Locate every malaria parasite.
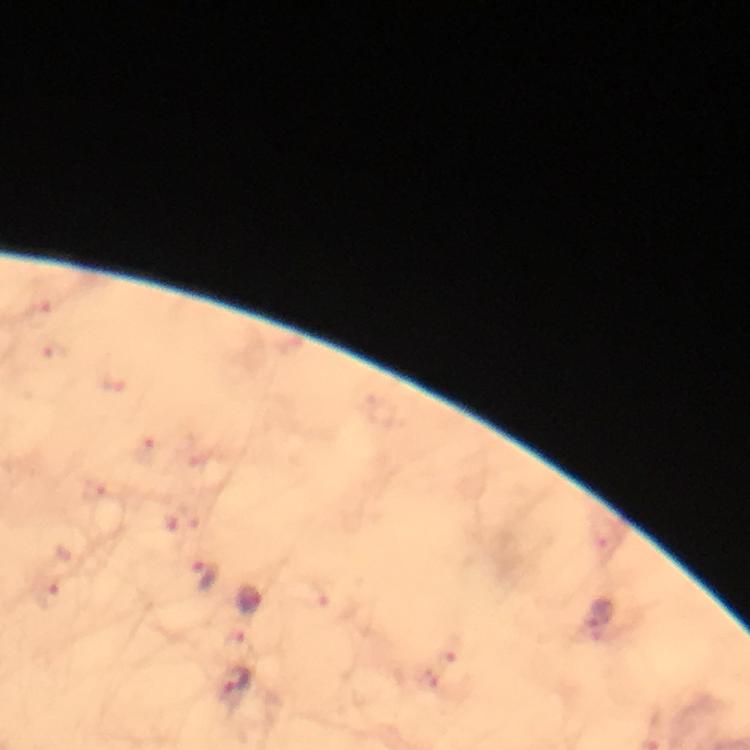
Approximate centers as (x, y) in pixels.
Malaria parasites: (205, 577), (248, 600), (599, 619), (235, 684).

Summary:
  - Magnification: 100x
  - Capture: smartphone mounted on the microscope
  - Preparation: thick blood film
  - Context: from a diagnostic examination for malaria
  - Image size: 750×750 pixels
  - Stain: Giemsa
  - Cropped from: one field of view
  - Immersion oil: used